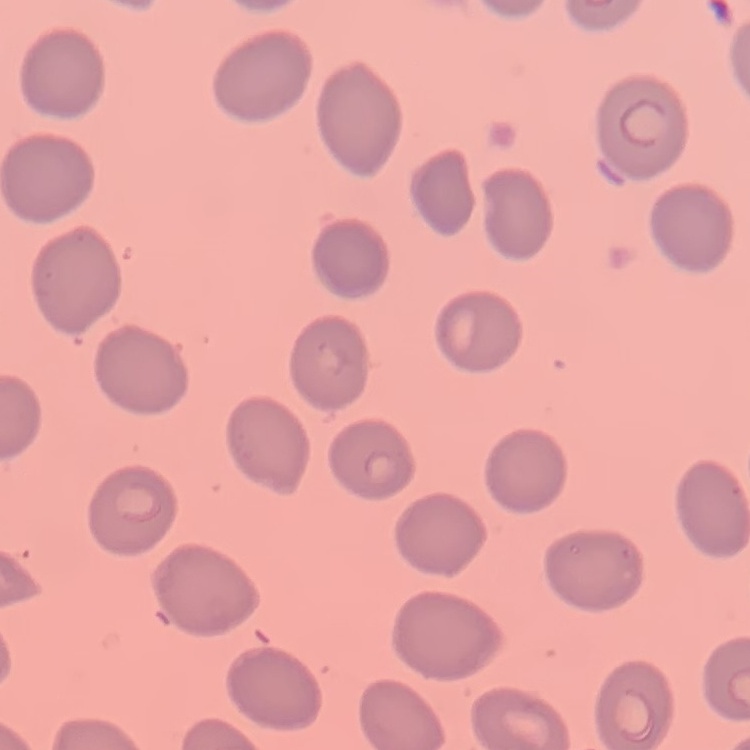

Summary:
  - Red blood cell morphology: no rouleaux formation
  - Preparation: thin peripheral smear
  - Stain: Field's or Giemsa
  - Image type: one tile cut from a larger photomicrograph